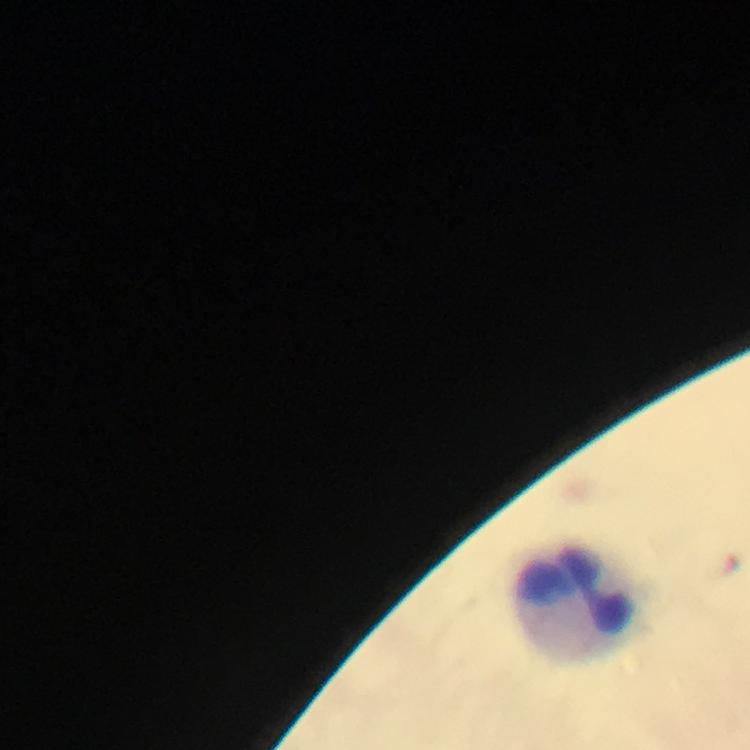

Approximate centers as {x, y} in pixels.
Summary:
  - Leukocyte locations: {583, 603}
  - Immersion oil: used
  - Stain: Giemsa
  - Preparation: thick blood smear
  - Context: from a malaria diagnostic workup
  - Magnification: 100x
  - Image size: 750×750 pixels
  - Malaria parasites: none seen
  - Capture: smartphone camera through the microscope
  - Cropped from: a single field of view